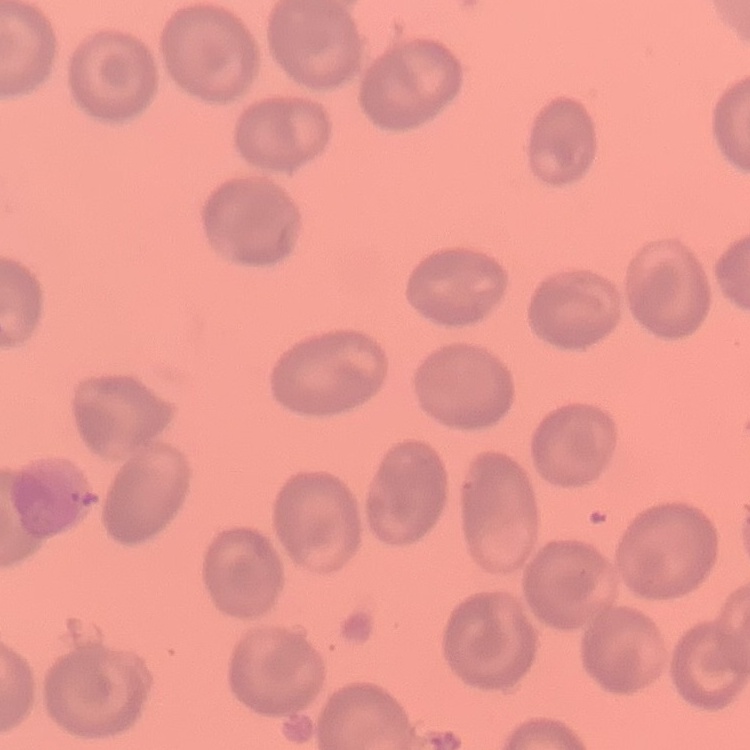
erythrocyte morphology = no rouleaux formation
stain = Field's or Giemsa
image type = square crop of a larger photomicrograph
preparation = thin blood smear